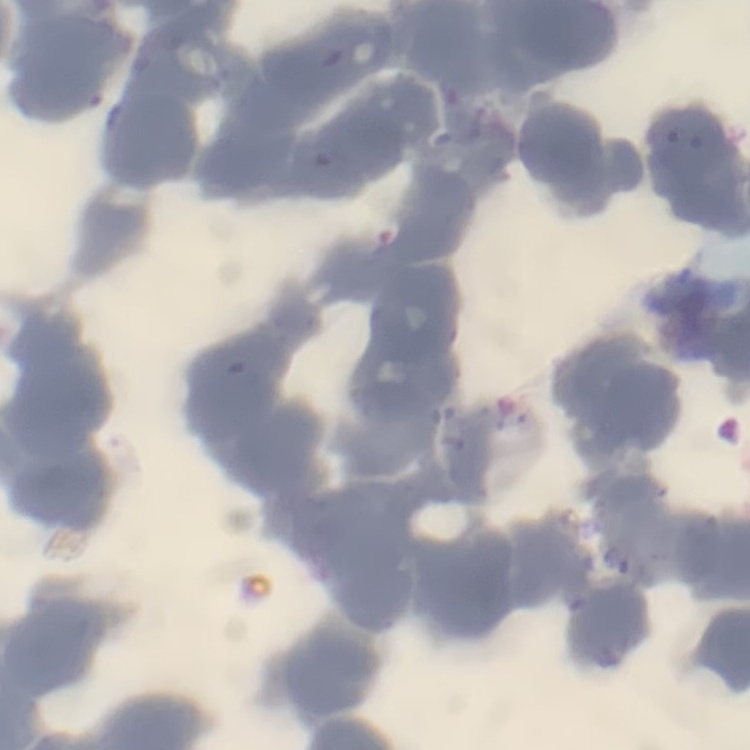 The red blood cells show rouleaux formation. Stained with either Field's or Giemsa. Thin peripheral smear. One tile cut from a larger photomicrograph.